Report the malaria status of this cell.
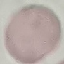

Uninfected.

Giemsa-stained preparation. Photographed with a smartphone camera at the microscope eyepiece. Cell patch, automatically extracted from a larger field of view and resized to 64 × 64 pixels. Thin blood film.